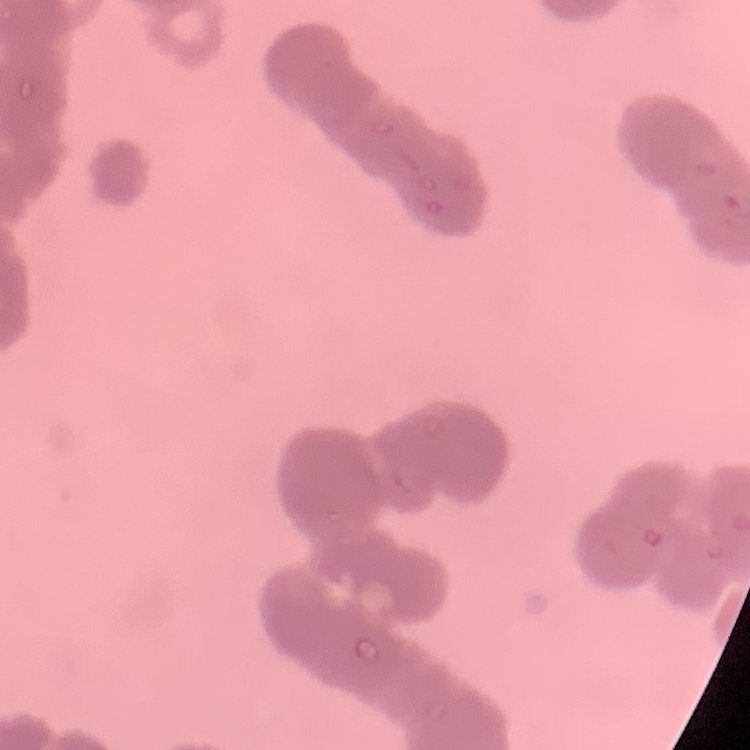
erythrocyte morphology = rouleaux formation
stain = Field's or Giemsa
image type = one tile cut from a larger photomicrograph
preparation = thin blood smear